Locate every blood parasite and identify its species.
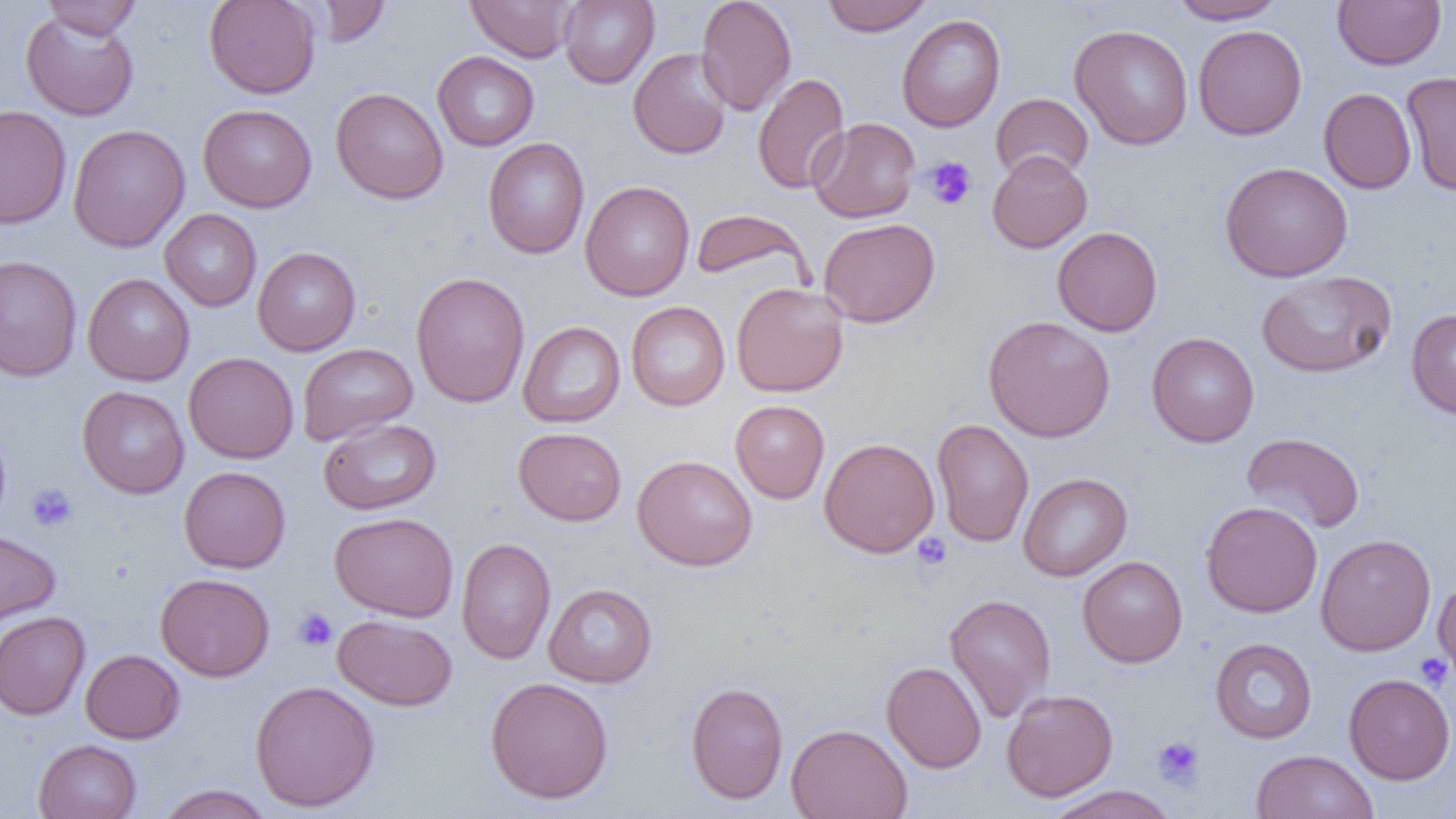

No blood parasites observed.

slide_level_diagnosis: negative for blood parasites
magnification: 1000x
field_of_view: one of a larger specimen
platelet_locations: 'approximate bounding boxes as (x1,y1)-(x2,y2) corner pairs in pixels: (923,156)-(976,210), (27,484)-(78,532), (912,532)-(952,571), (293,607)-(338,651), (1413,653)-(1453,691), (1152,736)-(1204,790)'
modality: optical microscopy
preparation: thin blood film
image_size: 1456×819 pixels
uninfected_red_blood_cell_locations: 'approximate bounding boxes as (x1,y1)-(x2,y2) corner pairs in pixels: (40,0)-(142,39), (204,0)-(320,99), (313,0)-(390,48), (465,0)-(578,62), (559,0)-(659,88), (696,0)-(796,116), (821,0)-(933,36), (1167,0)-(1287,24), (1332,0)-(1447,70), (20,9)-(139,121), (896,14)-(1006,132), (1069,24)-(1193,149), (1193,24)-(1307,140), (628,48)-(732,159), (432,51)-(539,151), (1401,71)-(1456,195), (752,72)-(850,194), (331,87)-(448,204), (1318,88)-(1416,194), (990,93)-(1094,183), (197,103)-(317,212), (0,105)-(71,229), (807,117)-(920,223), (68,124)-(190,252), (483,138)-(590,259), (987,150)-(1092,253), (1220,161)-(1353,282), (580,180)-(694,301), (690,208)-(811,287), (160,209)-(261,311), (818,218)-(940,327), (1052,226)-(1163,336), (252,246)-(360,356), (0,254)-(81,381), (1257,270)-(1396,378), (410,271)-(530,408), (82,273)-(195,386), (731,282)-(849,397), (626,301)-(730,411), (1406,309)-(1456,419), (983,315)-(1116,442), (518,321)-(626,427), (1147,332)-(1260,447), (297,343)-(418,445), (183,352)-(298,463), (77,386)-(189,498), (730,400)-(830,503), (318,418)-(441,515), (932,419)-(1033,545), (0,425)-(11,527), (513,426)-(627,526), (1241,432)-(1365,534), (819,437)-(939,557), (632,454)-(758,571), (179,466)-(290,573), (1018,472)-(1132,581), (1200,501)-(1323,618), (330,511)-(459,621), (0,528)-(61,628), (1315,534)-(1436,656), (456,537)-(556,665), (1077,556)-(1188,668), (155,573)-(275,681), (1433,577)-(1456,687), (543,583)-(657,688), (944,593)-(1056,722), (0,611)-(90,720), (332,614)-(458,711), (1209,638)-(1317,743), (80,649)-(185,743), (882,661)-(986,773), (1343,673)-(1456,784), (485,676)-(614,804), (249,679)-(380,812), (685,681)-(789,805), (1001,689)-(1118,802), (786,723)-(912,819), (33,739)-(141,819), (1251,750)-(1378,819), (157,784)-(274,819), (1043,785)-(1179,819)'